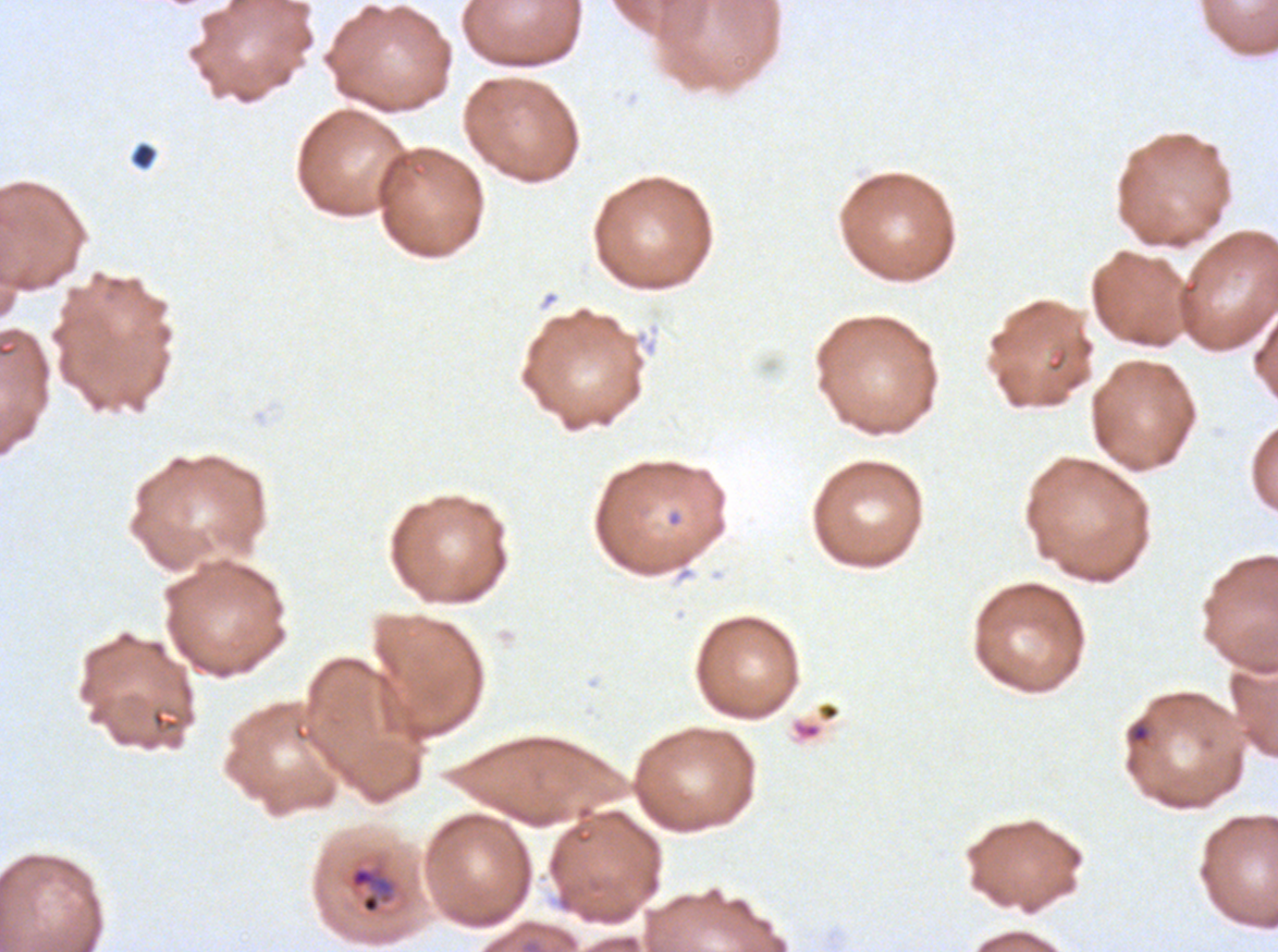
Approximate bounding boxes as {x1, y1, x2, y2} in pixels. Debris locations: {130, 142, 157, 170}. Ring locations: {1128, 721, 1151, 745}, {349, 866, 395, 914}. Image is 1278×952 pixels. Ex-vivo P. falciparum culture from a patient in The Gambia, grown for 24 to 48 hours. One sub-image of a larger composite. Thin blood film. Giemsa-stained preparation.